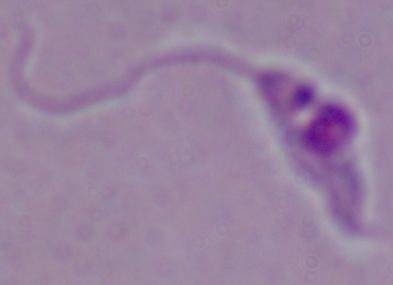

Summary:
  - Identification: Leishmania
  - Magnification: 1000x
  - Modality: photomicrograph